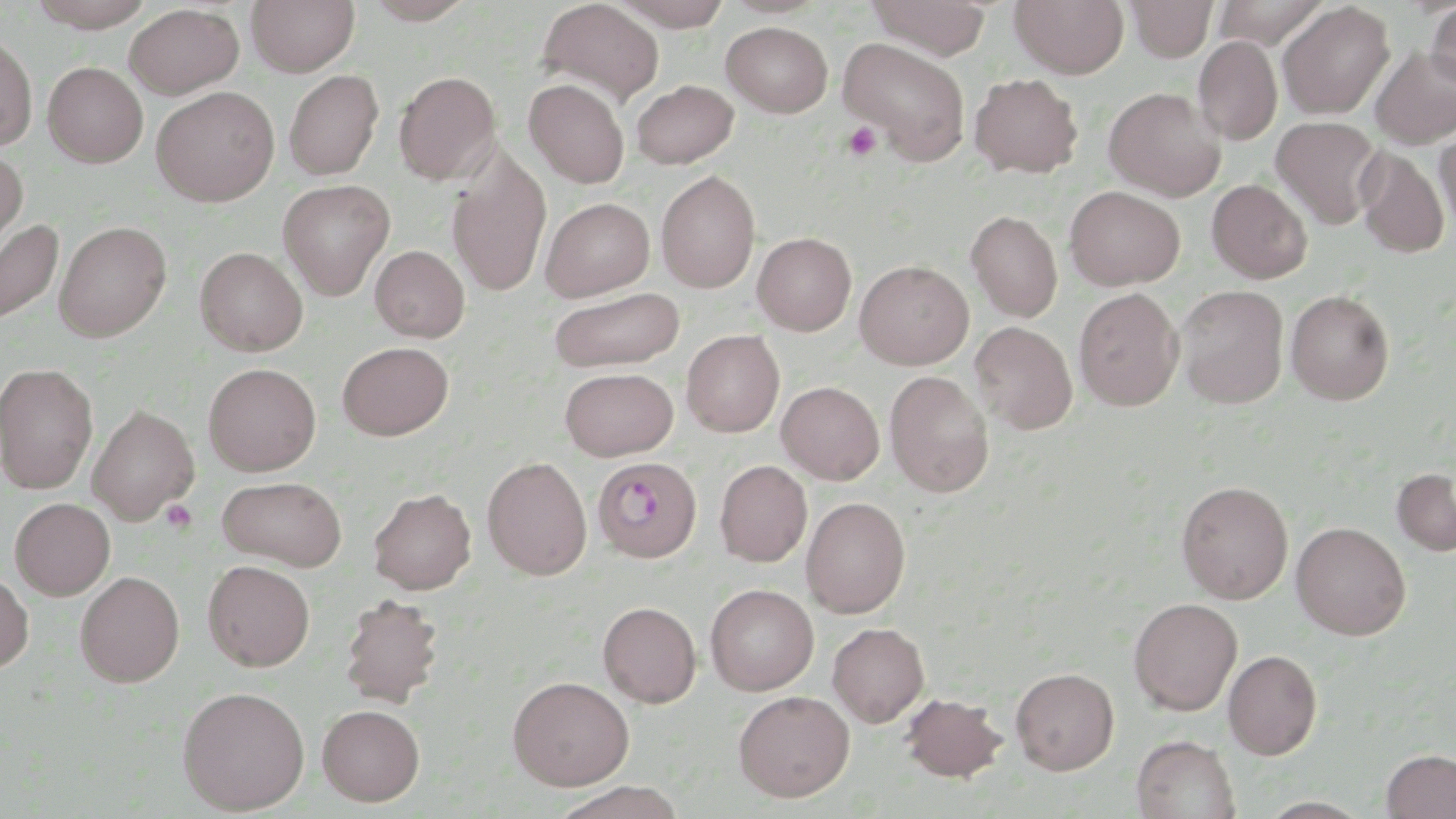
Summary:
  - Coordinate format: approximate bounding boxes as (x1,y1)-(x2,y2) corner pairs in pixels
  - Platelet locations: (842,121)-(883,162), (160,499)-(198,533)
  - Uninfected red blood cell locations: (24,0)-(158,30), (247,0)-(360,76), (361,0)-(477,24), (537,0)-(663,105), (611,0)-(734,30), (864,0)-(992,58), (1010,0)-(1129,77), (1127,0)-(1217,61), (1426,2)-(1456,92), (1278,3)-(1394,119), (124,5)-(244,98), (721,21)-(833,117), (0,30)-(37,151), (1194,36)-(1282,145), (837,37)-(970,162), (1370,46)-(1456,148), (42,61)-(148,167), (284,69)-(384,180), (394,71)-(501,184), (969,73)-(1083,178), (524,77)-(630,188), (631,79)-(739,168), (151,86)-(279,206), (1103,86)-(1225,200), (1271,116)-(1383,229), (1435,130)-(1456,234), (447,146)-(552,298), (1355,147)-(1449,258), (0,151)-(27,254), (657,169)-(760,292), (278,179)-(395,299), (1207,179)-(1311,283), (1065,186)-(1185,290), (542,197)-(655,301), (966,210)-(1063,321), (0,216)-(64,328), (54,220)-(172,342), (753,232)-(856,335), (370,245)-(470,343), (195,247)-(308,357), (855,260)-(973,369), (1175,285)-(1289,408), (548,287)-(685,373), (1074,287)-(1183,411), (1285,289)-(1395,405), (971,321)-(1078,434), (681,329)-(785,437), (337,341)-(454,440), (0,362)-(98,493), (203,363)-(321,475), (559,367)-(679,460), (885,370)-(994,496), (777,381)-(884,485), (88,404)-(198,523), (482,456)-(593,579), (715,460)-(812,567), (1392,467)-(1456,556), (216,475)-(348,571), (1176,480)-(1293,603), (368,487)-(476,594), (801,496)-(910,617), (10,497)-(114,599), (1291,521)-(1411,640), (202,559)-(315,671), (0,570)-(34,673), (76,571)-(184,686), (705,584)-(819,695), (338,594)-(445,706), (1129,597)-(1243,715), (598,601)-(701,707), (828,622)-(929,726), (1223,650)-(1322,759), (1011,667)-(1119,774), (508,676)-(634,790), (177,685)-(310,814), (733,690)-(855,802), (901,692)-(1008,782), (317,704)-(425,806), (1131,734)-(1240,819), (1381,748)-(1456,818), (550,782)-(688,819)
  - Slide-level diagnosis: no evidence of blood parasites
  - Field of view: single
  - Preparation: thin blood smear
  - Image size: 1456×819 pixels
  - Stain: May-Grünwald-Giemsa
  - Modality: optical microscopy
  - Magnification: 1000x